Point out each malaria parasite and classify it by life-cycle stage.
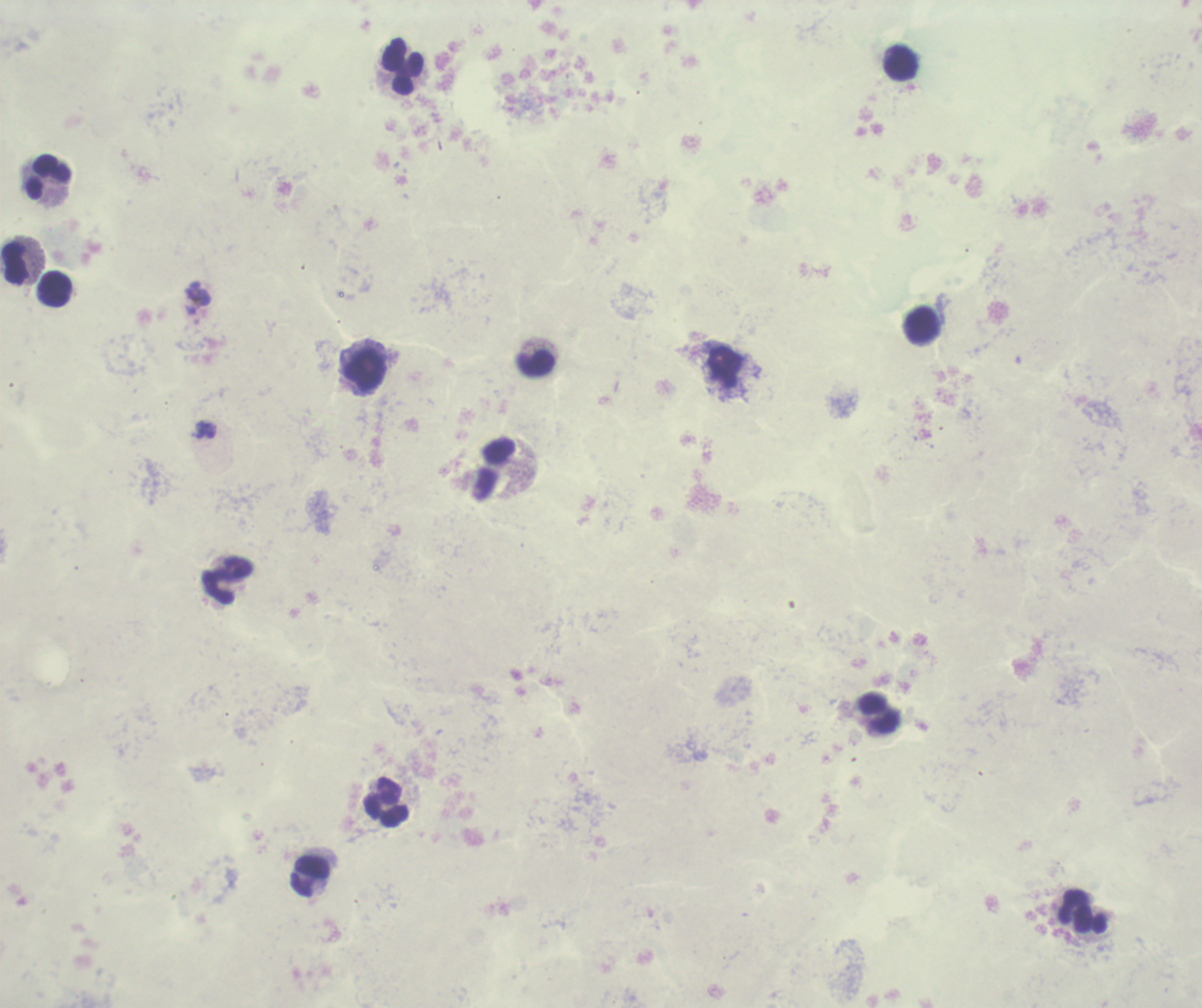

Approximate centers as [x, y] in pixels.
Trophozoites: [198, 294].
No schizont or gametocyte forms observed.

Approximate centers as [x, y] in pixels. Leukocyte locations: [901, 63], [403, 66], [49, 176], [16, 263], [55, 288], [919, 324], [537, 365], [366, 371], [227, 581], [387, 803], [310, 876], [1082, 912]. Coloration quality: bad. Image is 1202×1008 pixels. Previously used in an actual diagnosis. Captured at 100x magnification. Romanowsky-stained preparation. Thick smear of blood. One field from this slide. Background quality: poor.